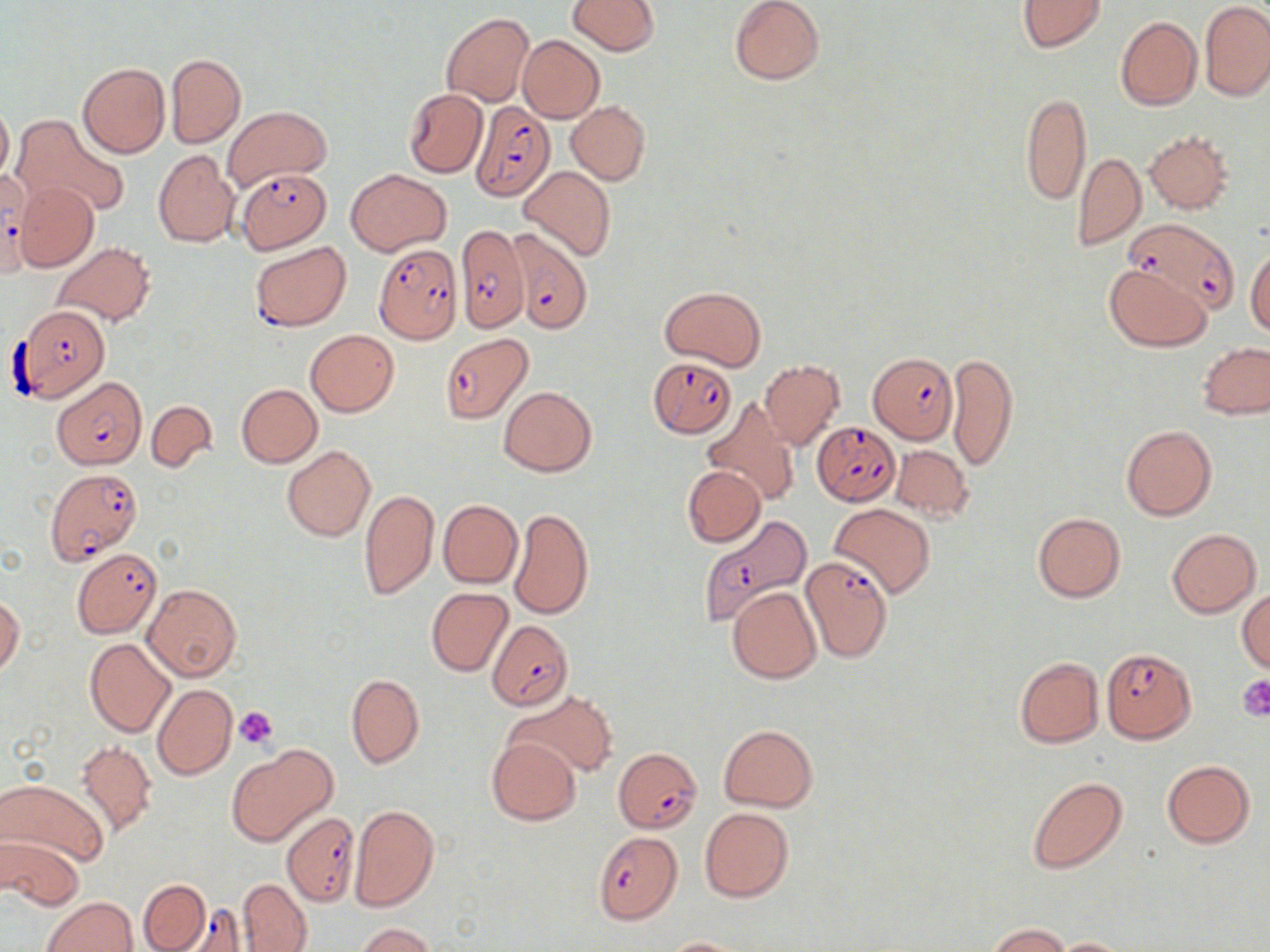
Summary:
  - Coordinate format: approximate bounding boxes as (x1, y1, x2, y2) in pixels
  - Platelet locations: (1236, 674, 1270, 719), (235, 706, 278, 748)
  - Uninfected red blood cell locations: (569, 0, 659, 55), (729, 0, 825, 86), (1017, 0, 1108, 53), (1200, 1, 1270, 101), (440, 13, 533, 106), (1115, 16, 1202, 110), (517, 35, 604, 123), (165, 52, 245, 148), (77, 62, 169, 157), (403, 87, 488, 178), (1019, 91, 1091, 208), (566, 100, 650, 185), (0, 102, 13, 184), (222, 106, 331, 189), (13, 115, 126, 218), (1144, 128, 1234, 213), (153, 149, 240, 248), (1073, 150, 1145, 250), (519, 165, 616, 262), (347, 168, 451, 256), (15, 181, 98, 272), (51, 242, 155, 327), (1246, 249, 1270, 339), (1105, 264, 1210, 351), (661, 285, 764, 372), (305, 329, 398, 416), (1198, 343, 1270, 419), (946, 351, 1019, 475), (758, 360, 844, 450), (236, 383, 323, 467), (499, 386, 597, 476), (703, 398, 800, 506), (146, 400, 216, 471), (1121, 424, 1216, 521), (281, 445, 375, 542), (890, 445, 974, 522), (682, 465, 765, 547), (359, 489, 439, 599), (438, 499, 522, 588), (829, 502, 936, 598), (507, 509, 592, 620), (1032, 512, 1125, 602), (1168, 528, 1261, 617), (142, 583, 241, 682), (727, 586, 821, 683), (1236, 586, 1270, 673), (426, 588, 513, 676), (0, 596, 24, 676), (85, 638, 176, 737), (1015, 656, 1103, 748), (346, 673, 424, 769), (152, 685, 237, 781), (508, 690, 617, 778), (173, 692, 279, 796), (718, 724, 817, 811), (486, 737, 582, 826), (76, 741, 157, 838), (226, 745, 338, 846), (1162, 760, 1255, 849), (1026, 777, 1126, 873), (1, 779, 108, 868), (350, 803, 439, 911), (699, 808, 794, 902), (1, 832, 85, 911), (138, 878, 210, 950), (239, 878, 311, 951), (42, 896, 137, 952), (987, 922, 1070, 951), (356, 923, 434, 952), (659, 937, 754, 951), (1049, 937, 1136, 951)
  - Plasmodium falciparum-infected red blood cell locations: (470, 102, 556, 202), (234, 168, 331, 252), (0, 172, 31, 273), (1125, 216, 1236, 315), (455, 224, 530, 332), (509, 231, 591, 332), (250, 241, 351, 331), (373, 245, 462, 344), (15, 305, 112, 403), (440, 334, 533, 422), (867, 351, 958, 444), (647, 356, 736, 438), (53, 376, 145, 469), (812, 420, 900, 505), (45, 467, 142, 566), (697, 513, 812, 627), (71, 547, 161, 637), (799, 556, 894, 663), (487, 620, 573, 710), (1102, 646, 1197, 743), (618, 749, 707, 834), (282, 811, 359, 906), (592, 832, 682, 924), (170, 904, 250, 951)
  - Slide-level diagnosis: Plasmodium falciparum
  - Preparation: thin blood film
  - Stain: May-Grünwald-Giemsa
  - Image size: 1270×952 pixels
  - Modality: optical microscopy
  - Magnification: 1000x
  - Field of view: single